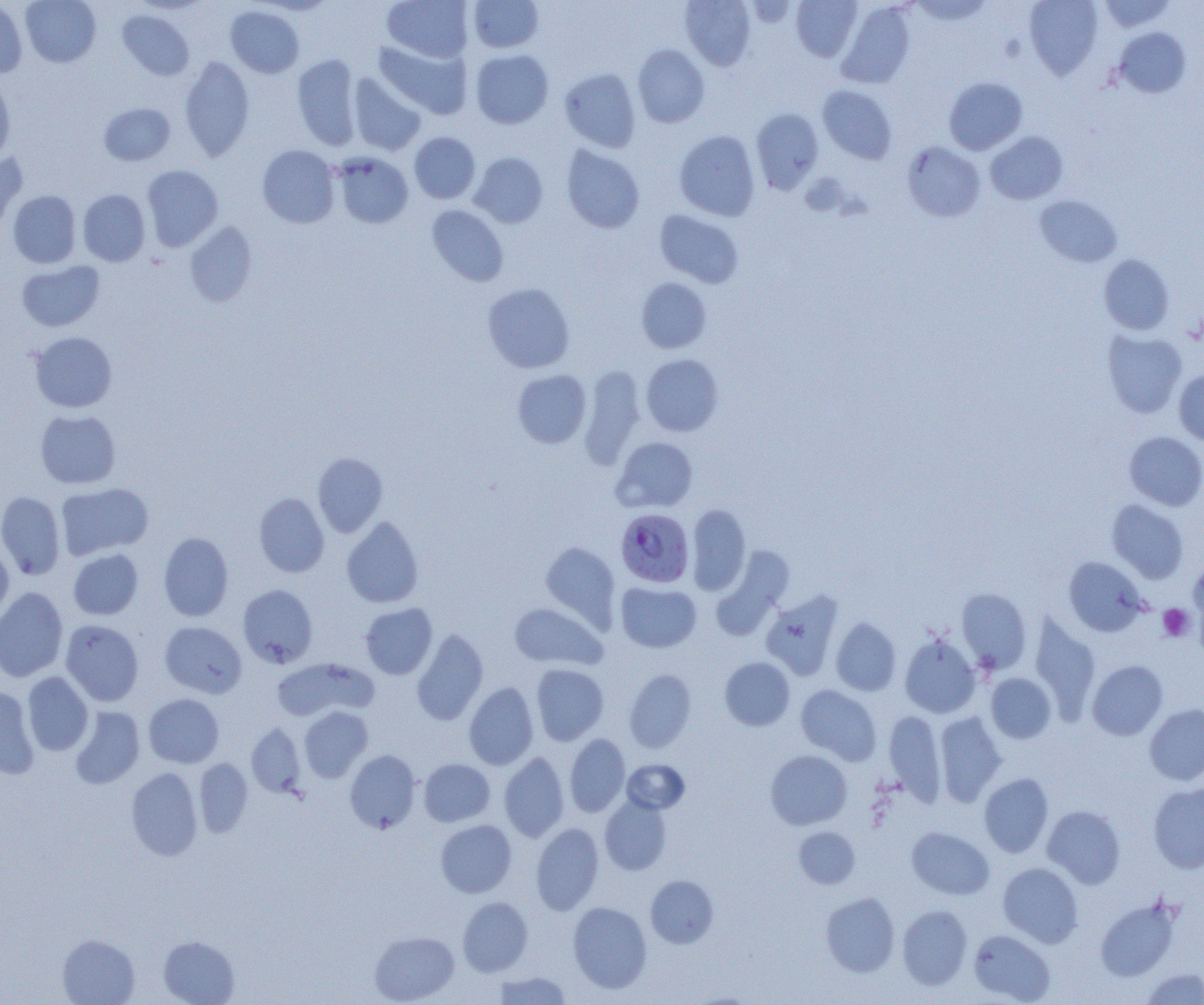

Plasmodium falciparum-infected red blood cell locations = approximate bounding boxes as [x1, y1, x2, y2] in pixels: [616, 508, 694, 587]
slide-level diagnosis = Plasmodium falciparum
uninfected red blood cell locations = approximate bounding boxes as [x1, y1, x2, y2] in pixels: [20, 0, 101, 68], [382, 0, 473, 62], [680, 0, 756, 70], [791, 0, 862, 61], [909, 0, 994, 26], [1024, 0, 1103, 79], [1098, 0, 1176, 33], [0, 1, 28, 78], [468, 1, 544, 53], [836, 2, 916, 88], [225, 6, 305, 78], [117, 10, 195, 81], [1113, 27, 1191, 98], [373, 39, 473, 120], [633, 44, 710, 128], [470, 49, 554, 129], [292, 53, 362, 151], [179, 56, 254, 161], [560, 68, 641, 152], [347, 73, 426, 155], [0, 76, 15, 164], [943, 77, 1027, 155], [818, 85, 898, 164], [99, 102, 175, 166], [751, 108, 824, 193], [674, 130, 760, 220], [985, 131, 1068, 205], [409, 132, 480, 204], [902, 141, 985, 221], [561, 144, 644, 233], [257, 145, 340, 228], [0, 152, 27, 235], [332, 152, 413, 228], [469, 152, 548, 228], [141, 165, 223, 251], [78, 189, 150, 266], [8, 190, 81, 268], [1034, 195, 1122, 267], [426, 205, 509, 286], [654, 209, 744, 288], [184, 222, 258, 307], [1098, 254, 1175, 335], [17, 260, 104, 332], [636, 278, 711, 353], [482, 282, 575, 373], [1101, 329, 1187, 418], [30, 332, 117, 412], [641, 353, 724, 436], [578, 365, 646, 469], [512, 369, 591, 448], [1174, 369, 1204, 447], [35, 410, 121, 489], [1124, 431, 1204, 511], [611, 437, 698, 513], [312, 452, 388, 537], [56, 483, 154, 560], [0, 491, 66, 580], [254, 492, 330, 578], [1107, 499, 1188, 584], [686, 504, 751, 595], [341, 517, 424, 608], [159, 532, 234, 621], [0, 541, 13, 623], [540, 541, 621, 628], [712, 546, 793, 639], [68, 548, 143, 620], [1063, 557, 1148, 636], [1188, 557, 1204, 642], [616, 581, 702, 653], [238, 585, 318, 668], [0, 587, 68, 682], [956, 588, 1032, 673], [761, 590, 844, 680], [509, 602, 607, 671], [360, 603, 437, 679], [1030, 614, 1100, 719], [830, 617, 901, 696], [61, 620, 144, 706], [160, 621, 247, 698], [411, 629, 489, 725], [899, 634, 981, 717], [271, 657, 378, 721], [719, 657, 795, 731], [1087, 660, 1168, 740], [531, 664, 609, 746], [624, 669, 697, 752], [23, 672, 93, 756], [986, 673, 1056, 743], [463, 682, 539, 770], [796, 685, 882, 764], [0, 686, 40, 779], [144, 694, 224, 768], [1144, 704, 1204, 786], [69, 706, 145, 789], [299, 706, 373, 782], [884, 711, 946, 803], [934, 712, 1007, 806], [246, 724, 306, 797], [565, 733, 630, 817], [344, 750, 421, 833], [765, 750, 852, 830], [499, 752, 570, 842], [194, 758, 253, 837], [419, 759, 495, 827], [622, 759, 690, 814], [139, 762, 250, 843], [126, 767, 203, 860], [979, 773, 1054, 858], [1148, 783, 1204, 873], [599, 796, 672, 874], [1042, 805, 1125, 888], [436, 819, 516, 897], [531, 823, 604, 915], [794, 826, 860, 888], [906, 827, 995, 899], [998, 862, 1083, 947], [646, 875, 719, 949], [821, 892, 901, 977], [458, 897, 533, 976], [1095, 897, 1180, 981], [568, 901, 652, 993], [897, 904, 972, 989], [968, 929, 1055, 1004], [369, 931, 459, 1004], [57, 934, 140, 1005], [158, 936, 240, 1005], [1140, 968, 1204, 1004], [493, 971, 572, 1004]
field of view = one of a larger specimen
image size = 1204×1005 pixels
platelet locations = approximate bounding boxes as [x1, y1, x2, y2] in pixels: [1159, 603, 1194, 642]
preparation = thin blood film
magnification = 1000x
modality = optical microscopy